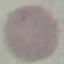

Summary:
  - Malaria status: uninfected
  - Capture: smartphone camera at the microscope eyepiece
  - Stain: Giemsa
  - Preparation: thin blood smear
  - Image type: automatically extracted cell patch, resized to 64 × 64 pixels